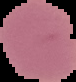
image_size: 76×82 pixels
image_type: cell region segmented out of the field of view; surrounding area masked to black
preparation: thin blood film
malaria_status: uninfected